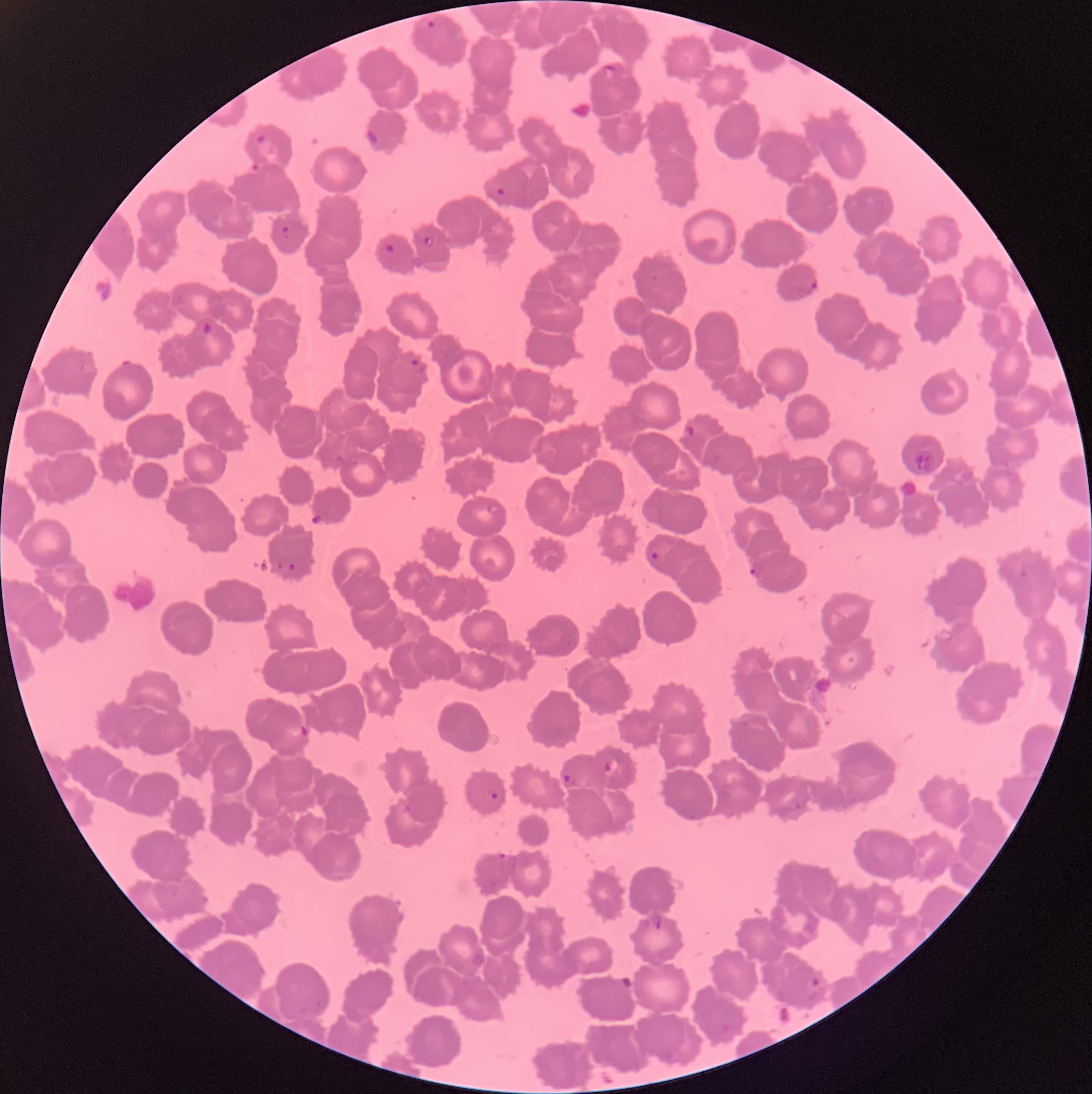
Summary:
  - Coordinate format: approximate bounding boxes as (x1,y1)-(x2,y2) corner pairs in pixels
  - Plasmodium parasite locations: (424,20)-(439,31), (602,63)-(618,81), (364,128)-(381,146), (255,134)-(266,144), (251,160)-(261,175), (494,187)-(506,197), (280,224)-(291,239), (423,236)-(435,248), (384,242)-(396,255), (793,281)-(818,294), (203,321)-(213,335), (410,357)-(425,373), (684,426)-(695,436), (646,549)-(661,562), (277,561)-(298,572), (749,561)-(767,582), (300,724)-(309,736), (604,756)-(620,774), (563,771)-(576,786), (488,788)-(499,800), (498,850)-(508,861), (647,910)-(665,931), (805,977)-(820,996)
  - Image size: 1092×1094 pixels
  - Red blood cell morphology: rouleaux formation
  - Preparation: thin blood smear
  - Modality: optical microscopy